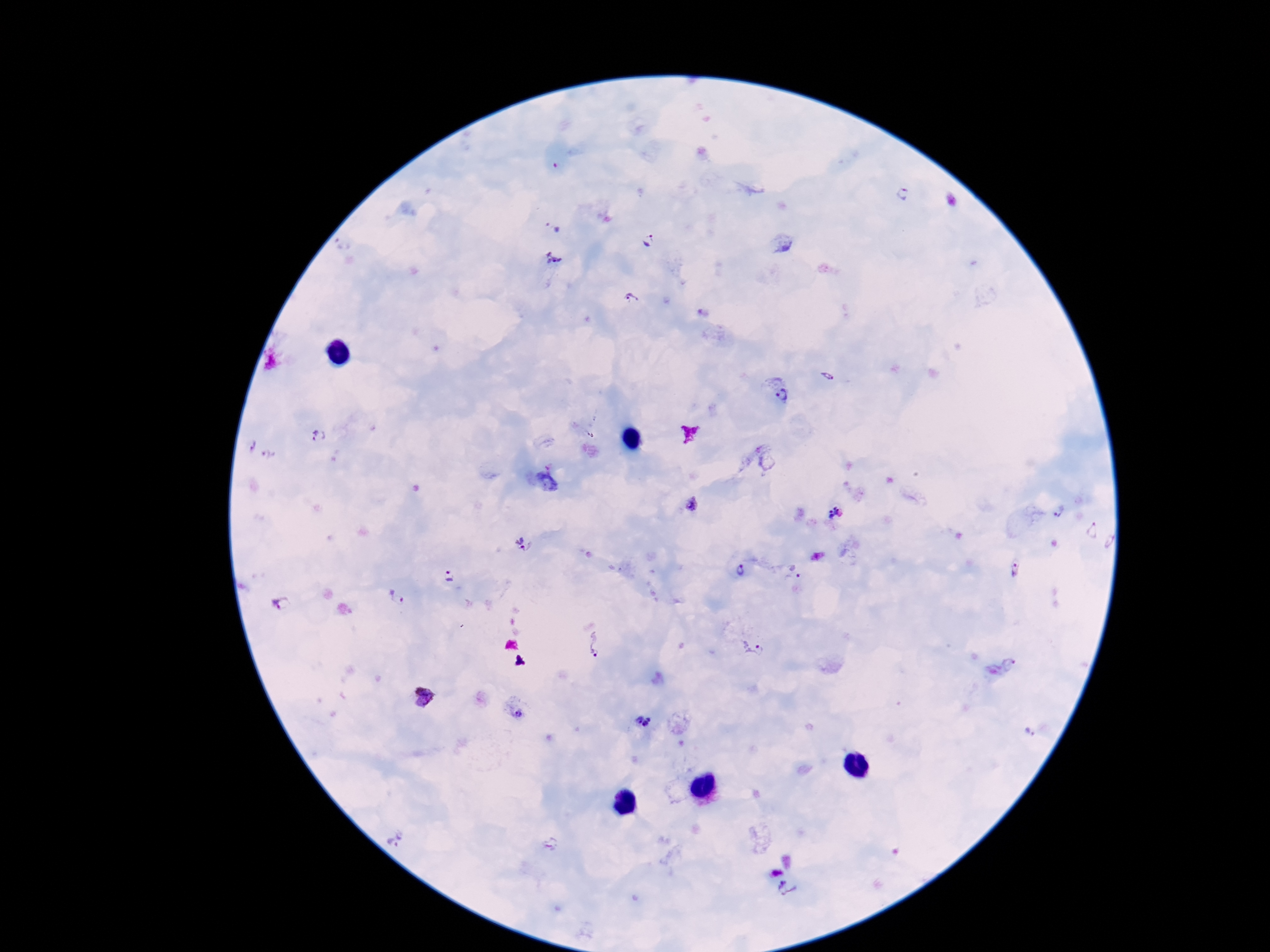

Plasmodium parasite locations = approximate object centers, in pixels from the top-left corner: (x=904, y=192), (x=647, y=242), (x=555, y=258), (x=632, y=299), (x=827, y=376), (x=779, y=388), (x=319, y=437), (x=250, y=447), (x=692, y=505), (x=1058, y=512), (x=835, y=514), (x=1093, y=531), (x=524, y=545), (x=1015, y=568), (x=741, y=570), (x=799, y=575), (x=449, y=577), (x=396, y=597), (x=281, y=604), (x=596, y=645), (x=754, y=649), (x=520, y=715), (x=643, y=722), (x=1029, y=731), (x=396, y=838), (x=789, y=890)
patient malaria status = positive
image size = 1270×952 pixels
stain = Giemsa
magnification = 100x
preparation = thick blood film
field of view = single
capture = smartphone camera through the microscope eyepiece